Identify the blood parasite species.
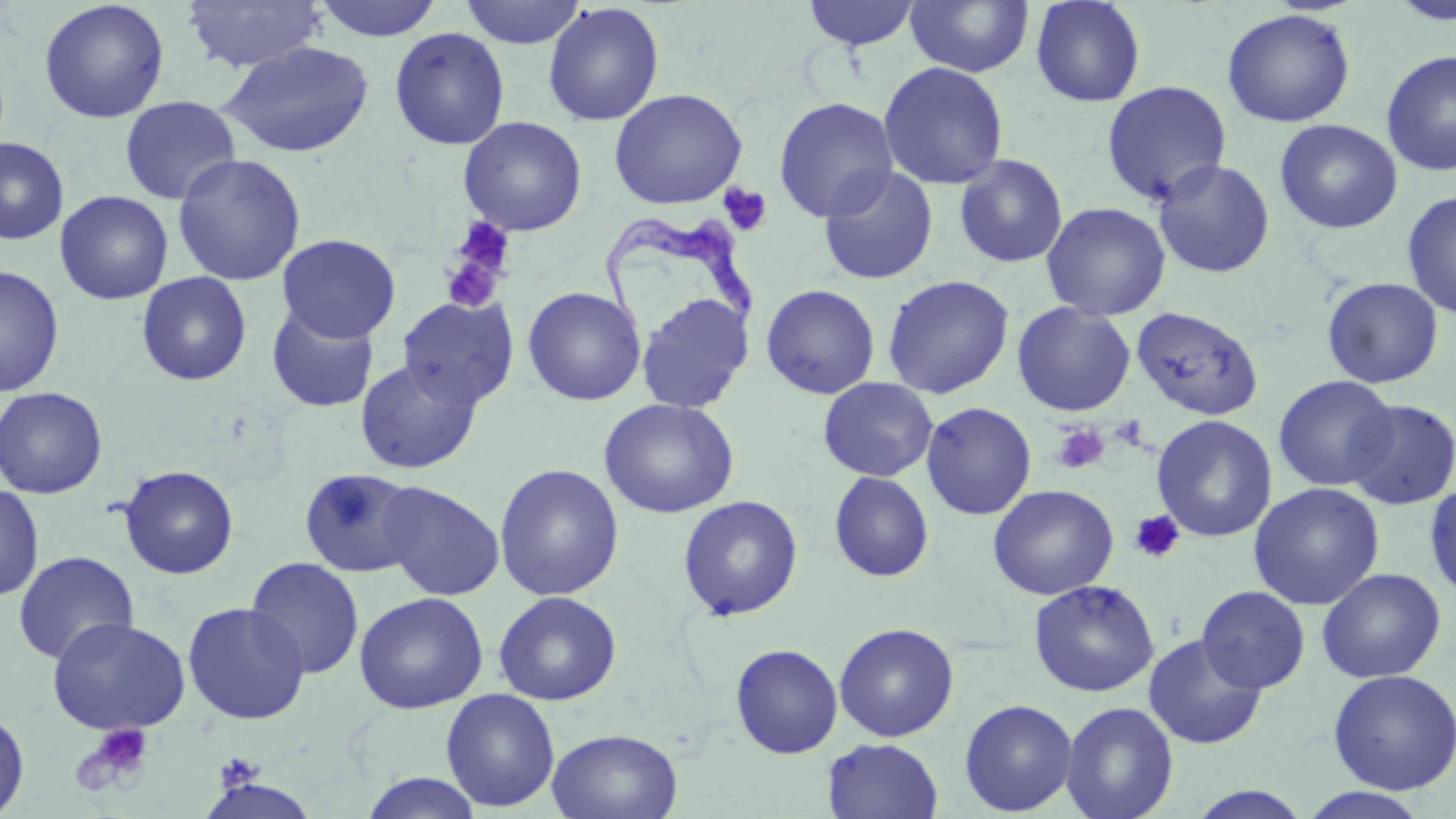
Trypanosoma brucei.

Approximate bounding boxes as named x1/y1/x2/y2 corners in pixels. Uninfected red blood cell locations: (x1=181, y1=0, x2=327, y2=73), (x1=312, y1=0, x2=443, y2=41), (x1=459, y1=0, x2=586, y2=48), (x1=1030, y1=0, x2=1147, y2=108), (x1=1387, y1=0, x2=1456, y2=26), (x1=38, y1=1, x2=170, y2=124), (x1=801, y1=1, x2=922, y2=50), (x1=905, y1=1, x2=1034, y2=78), (x1=543, y1=2, x2=664, y2=126), (x1=1221, y1=8, x2=1356, y2=127), (x1=389, y1=27, x2=510, y2=150), (x1=220, y1=41, x2=375, y2=158), (x1=1381, y1=50, x2=1456, y2=176), (x1=877, y1=61, x2=1009, y2=190), (x1=1101, y1=80, x2=1232, y2=206), (x1=608, y1=88, x2=747, y2=209), (x1=119, y1=95, x2=241, y2=205), (x1=774, y1=96, x2=898, y2=222), (x1=458, y1=116, x2=587, y2=235), (x1=1275, y1=119, x2=1403, y2=234), (x1=0, y1=136, x2=69, y2=245), (x1=172, y1=153, x2=306, y2=286), (x1=954, y1=153, x2=1068, y2=268), (x1=1153, y1=159, x2=1275, y2=279), (x1=819, y1=167, x2=939, y2=286), (x1=1402, y1=190, x2=1456, y2=320), (x1=55, y1=191, x2=173, y2=305), (x1=1040, y1=201, x2=1171, y2=321), (x1=276, y1=233, x2=401, y2=343), (x1=0, y1=265, x2=65, y2=398), (x1=136, y1=271, x2=253, y2=386), (x1=882, y1=274, x2=1015, y2=399), (x1=1322, y1=277, x2=1444, y2=389), (x1=760, y1=283, x2=881, y2=399), (x1=522, y1=286, x2=646, y2=406), (x1=635, y1=291, x2=755, y2=413), (x1=398, y1=295, x2=519, y2=408), (x1=1012, y1=301, x2=1136, y2=416), (x1=266, y1=302, x2=379, y2=413), (x1=1132, y1=306, x2=1263, y2=421), (x1=355, y1=358, x2=482, y2=474), (x1=1273, y1=375, x2=1398, y2=491), (x1=818, y1=377, x2=939, y2=482), (x1=0, y1=386, x2=108, y2=499), (x1=599, y1=398, x2=739, y2=518), (x1=1344, y1=398, x2=1456, y2=510), (x1=921, y1=401, x2=1037, y2=520), (x1=1151, y1=415, x2=1278, y2=542), (x1=493, y1=464, x2=625, y2=601), (x1=118, y1=465, x2=239, y2=579), (x1=298, y1=468, x2=422, y2=578), (x1=829, y1=471, x2=934, y2=582), (x1=376, y1=481, x2=505, y2=600), (x1=1248, y1=482, x2=1385, y2=611), (x1=1424, y1=482, x2=1456, y2=604), (x1=0, y1=483, x2=44, y2=602), (x1=988, y1=484, x2=1119, y2=600), (x1=677, y1=495, x2=804, y2=621), (x1=13, y1=550, x2=139, y2=665), (x1=245, y1=556, x2=365, y2=678), (x1=1317, y1=567, x2=1446, y2=683), (x1=1029, y1=579, x2=1160, y2=697), (x1=1197, y1=585, x2=1310, y2=693), (x1=493, y1=590, x2=622, y2=705), (x1=353, y1=591, x2=488, y2=714), (x1=182, y1=601, x2=310, y2=725), (x1=46, y1=616, x2=190, y2=736), (x1=834, y1=623, x2=959, y2=742), (x1=1144, y1=633, x2=1268, y2=749), (x1=730, y1=643, x2=843, y2=758), (x1=1327, y1=668, x2=1456, y2=795), (x1=441, y1=688, x2=560, y2=812), (x1=959, y1=698, x2=1078, y2=816), (x1=1060, y1=701, x2=1179, y2=819), (x1=0, y1=707, x2=30, y2=817), (x1=547, y1=727, x2=683, y2=819), (x1=821, y1=738, x2=943, y2=819), (x1=358, y1=772, x2=485, y2=818), (x1=1182, y1=785, x2=1315, y2=818), (x1=1297, y1=787, x2=1433, y2=819). Trypanosoma brucei locations: (x1=601, y1=212, x2=761, y2=327). Platelet locations: (x1=718, y1=183, x2=773, y2=236), (x1=443, y1=218, x2=518, y2=302), (x1=1111, y1=416, x2=1147, y2=449), (x1=1052, y1=423, x2=1110, y2=474), (x1=1129, y1=510, x2=1185, y2=564), (x1=89, y1=724, x2=153, y2=781), (x1=216, y1=752, x2=263, y2=788). 1000x magnification. Image is 1456×819 pixels. One field of a larger specimen. Thin blood smear. Light microscopy. May-Grünwald-Giemsa-stained preparation.